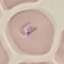
Summary:
  - Result: malaria parasites identified
  - Stain: Giemsa
  - Image type: cell patch, automatically extracted from a larger field of view and resized to 64 × 64 pixels
  - Preparation: thin blood smear
  - Capture: smartphone camera at the microscope eyepiece